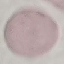 Result: no malaria parasites detected. Acquired by smartphone through the microscope eyepiece. Giemsa stain. Automatically extracted cell patch, resized to 64 × 64 pixels. Thin blood smear.